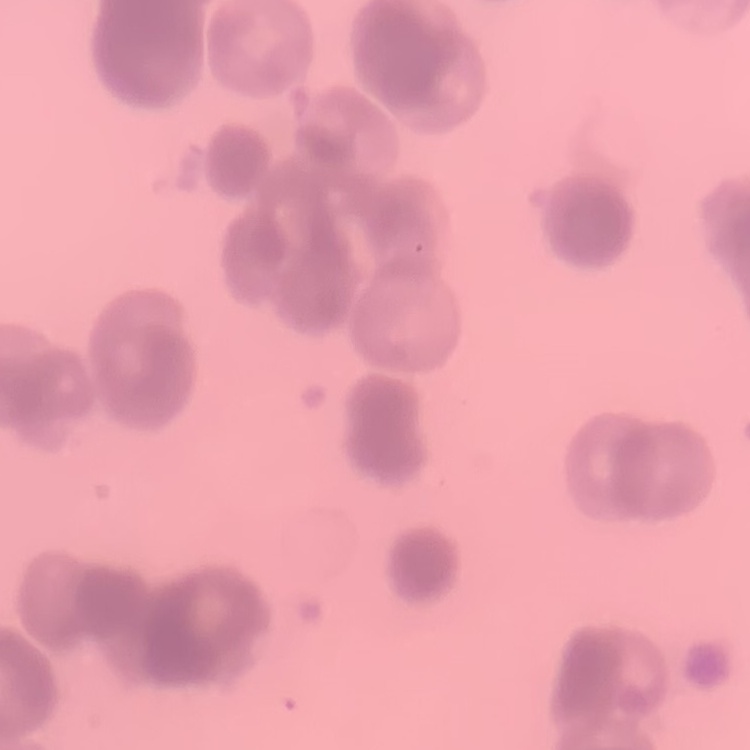
The erythrocytes show rouleaux formation. Thin peripheral smear. One tile cut from a larger photomicrograph. Stained with either Field's or Giemsa.